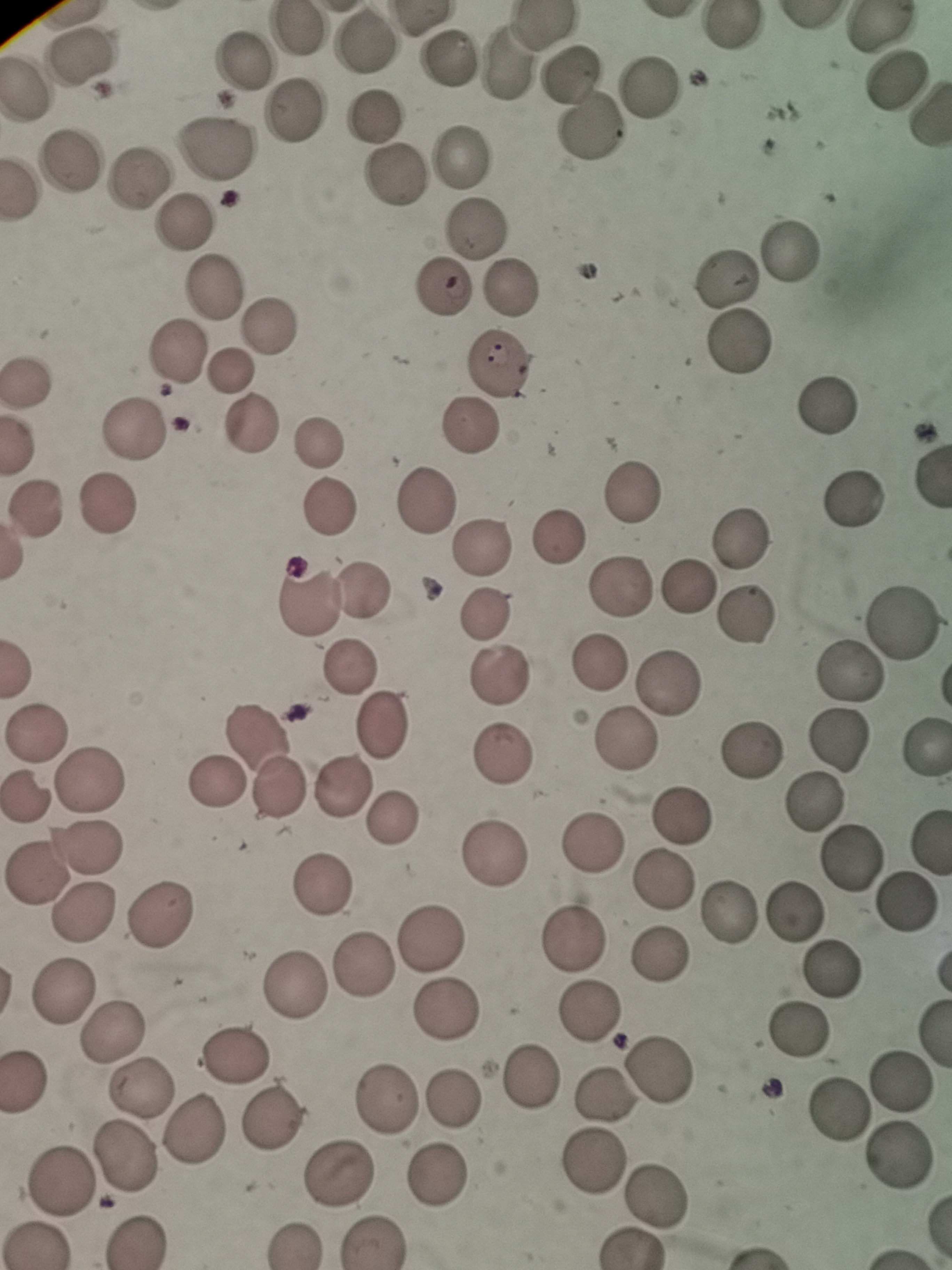 Approximate centers as {x, y} in pixels. Cell locations: {297, 30}, {366, 40}, {443, 57}, {79, 59}, {506, 62}, {244, 63}, {571, 75}, {23, 86}, {648, 86}, {289, 114}, {373, 119}, {592, 126}, {214, 148}, {74, 155}, {460, 160}, {395, 175}, {137, 180}, {185, 225}, {481, 227}, {793, 251}, {727, 279}, {213, 287}, {513, 290}, {440, 294}, {269, 326}, {737, 345}, {173, 356}, {500, 363}, {231, 370}, {23, 380}, {830, 399}, {254, 425}, {469, 428}, {134, 431}, {319, 432}, {630, 494}, {430, 497}, {854, 501}, {328, 503}, {36, 506}, {106, 506}, {744, 534}, {557, 535}, {486, 542}, {689, 584}, {619, 586}, {369, 588}, {305, 606}, {487, 607}, {743, 614}, {903, 618}, {597, 661}, {350, 663}, {847, 671}, {498, 673}, {667, 679}, {387, 720}, {36, 731}, {260, 731}, {626, 738}, {837, 738}, {500, 748}, {923, 748}, {751, 749}, {96, 770}, {216, 785}, {282, 785}, {342, 786}, {26, 794}, {813, 800}, {399, 815}, {684, 815}, {87, 844}, {595, 847}, {495, 854}, {849, 857}, {35, 875}, {664, 881}, {320, 885}, {907, 904}, {162, 909}, {84, 911}, {728, 911}, {794, 911}, {428, 937}, {575, 939}, {659, 957}, {363, 968}, {830, 969}, {295, 981}, {61, 985}, {446, 1005}, {590, 1013}, {115, 1026}, {795, 1031}, {237, 1056}, {659, 1068}, {24, 1075}, {529, 1075}, {899, 1081}, {138, 1088}, {386, 1093}, {604, 1096}, {451, 1098}, {837, 1111}, {268, 1116}, {194, 1131}, {123, 1156}, {898, 1156}, {593, 1161}, {338, 1173}, {439, 1176}, {58, 1178}, {652, 1196}, {140, 1238}, {380, 1239}, {38, 1242}, {291, 1244}. Thin smear of blood. Giemsa stain. One field from this slide. Image is 952×1270 pixels. Photographed with a smartphone camera at the microscope eyepiece.